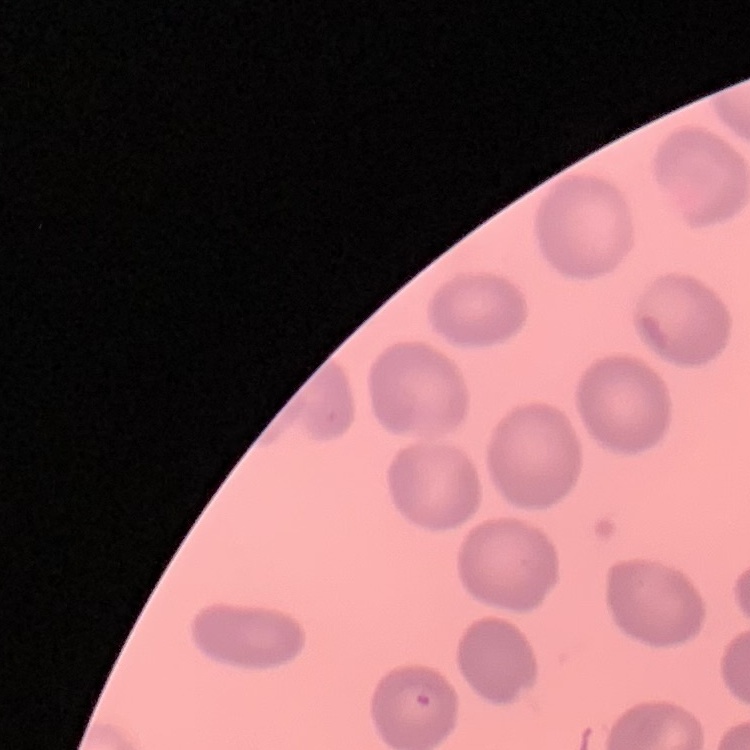
Summary:
  - Erythrocyte morphology: no rouleaux formation
  - Stain: Field's or Giemsa
  - Preparation: thin blood film
  - Image type: one tile cut from a larger photomicrograph